Give the location of every white blood cell.
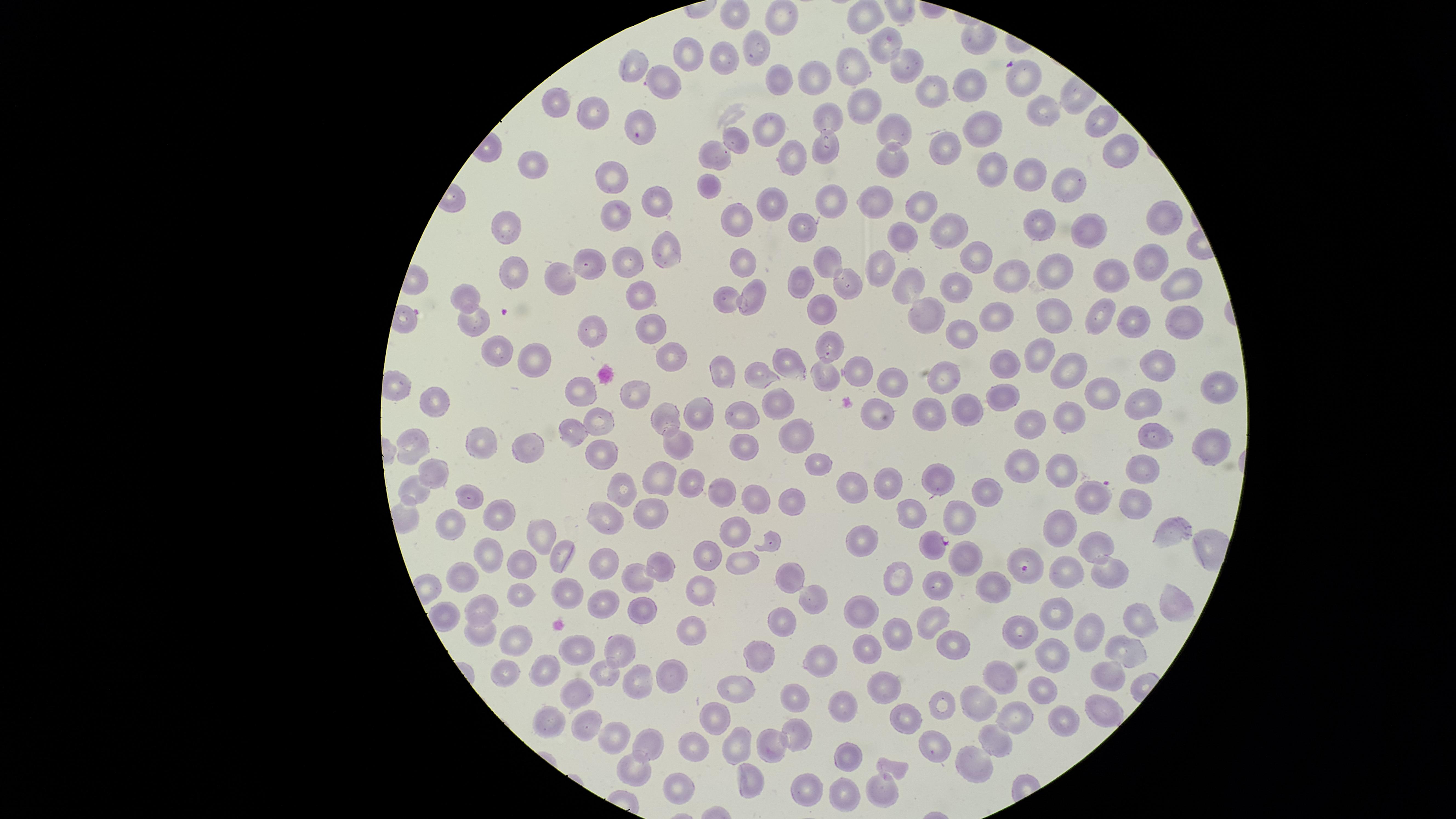
No white blood cells identified.

presence: malaria parasites seen
field_of_view: single
parasitized_red_blood_cells: 'approximate marker points as [x, y] in pixels: [1093, 498], [934, 544], [1025, 568]'
uninfected_red_blood_cells: 'approximate marker points as [x, y] in pixels: [781, 18], [862, 18], [885, 45], [762, 47], [724, 55], [686, 56], [905, 66], [636, 69], [858, 69], [813, 73], [667, 80], [779, 82], [969, 82], [1025, 82], [930, 85], [556, 106], [865, 106], [1043, 110], [593, 111], [638, 119], [828, 119], [1098, 123], [977, 125], [896, 129], [767, 130], [735, 139], [941, 143], [822, 147], [1114, 149], [719, 156], [788, 158], [892, 158], [532, 165], [991, 173], [612, 176], [1029, 179], [709, 182], [1068, 186], [831, 197], [656, 202], [881, 202], [772, 205], [919, 205], [618, 219], [735, 219], [1162, 219], [804, 225], [1044, 226], [510, 227], [948, 227], [1091, 234], [901, 236], [667, 251], [827, 260], [631, 261], [974, 262], [588, 263], [742, 264], [1142, 265], [514, 270], [883, 270], [1054, 272], [1108, 273], [563, 275], [1007, 276], [907, 281], [954, 282], [1182, 283], [802, 284], [845, 287], [750, 288], [641, 293], [466, 298], [725, 298], [931, 311], [823, 313], [1002, 316], [1096, 318], [1057, 319], [1133, 321], [475, 322], [1176, 323], [650, 324], [594, 329], [959, 331], [831, 342], [493, 349], [666, 352], [1038, 352], [528, 359], [785, 361], [1004, 362], [1151, 365], [722, 368], [1068, 370], [824, 371], [760, 374], [856, 375], [892, 379], [942, 381], [1215, 386], [584, 390], [636, 393], [1096, 393], [993, 397], [775, 399], [436, 402], [1132, 407], [694, 410], [933, 412], [970, 413], [736, 414], [877, 415], [665, 419], [1065, 421], [598, 422], [1023, 424], [571, 429], [795, 439], [1151, 439], [480, 441], [1209, 441], [416, 445], [676, 447], [528, 448], [740, 454], [606, 455], [815, 464], [1060, 467], [1143, 467], [1021, 469], [662, 470], [437, 472], [690, 479], [936, 480], [887, 484], [719, 486], [851, 487], [417, 488], [624, 492], [982, 493], [752, 499], [469, 501], [787, 503], [1135, 503], [654, 510], [905, 510], [493, 515], [602, 516], [957, 516], [450, 522], [1066, 528], [1173, 529], [538, 533], [730, 533], [864, 542], [1103, 543], [485, 549], [964, 552], [559, 555], [707, 556], [604, 558], [743, 562], [525, 563], [658, 565], [1064, 570], [463, 576], [785, 576], [1102, 577], [637, 578], [897, 582], [698, 586], [938, 588], [1002, 588], [562, 593], [523, 595], [600, 598], [813, 599], [1170, 605], [640, 607], [481, 611], [858, 612], [1061, 616], [931, 618], [1131, 620], [779, 626], [695, 631], [1083, 631], [477, 632], [899, 632], [1025, 632], [515, 641], [952, 642], [575, 647], [1120, 648], [616, 651], [865, 651], [1058, 653], [760, 655], [819, 661], [502, 668], [1110, 669], [1004, 672], [542, 674], [676, 676], [602, 677], [640, 685], [877, 687], [731, 688], [1042, 690], [575, 696], [788, 699], [938, 699], [839, 702], [979, 702], [1098, 707], [712, 712], [910, 714], [1016, 715], [553, 721], [1060, 725], [588, 726], [612, 730], [797, 733], [997, 739], [689, 744], [743, 744], [769, 746], [937, 749], [646, 750], [851, 758], [967, 759], [893, 767], [631, 770], [749, 776], [672, 791], [796, 793], [879, 793], [841, 795]'
capture: smartphone photograph through the microscope eyepiece
stain: Giemsa
image_size: 1456×819 pixels
preparation: thin blood film
visible_region: circular
species: Plasmodium falciparum